Assess this cell for malaria.
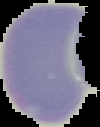

It is uninfected.

preparation: thin blood smear
image_type: cell region segmented out of the field of view; surrounding area masked to black
image_size: 100×127 pixels